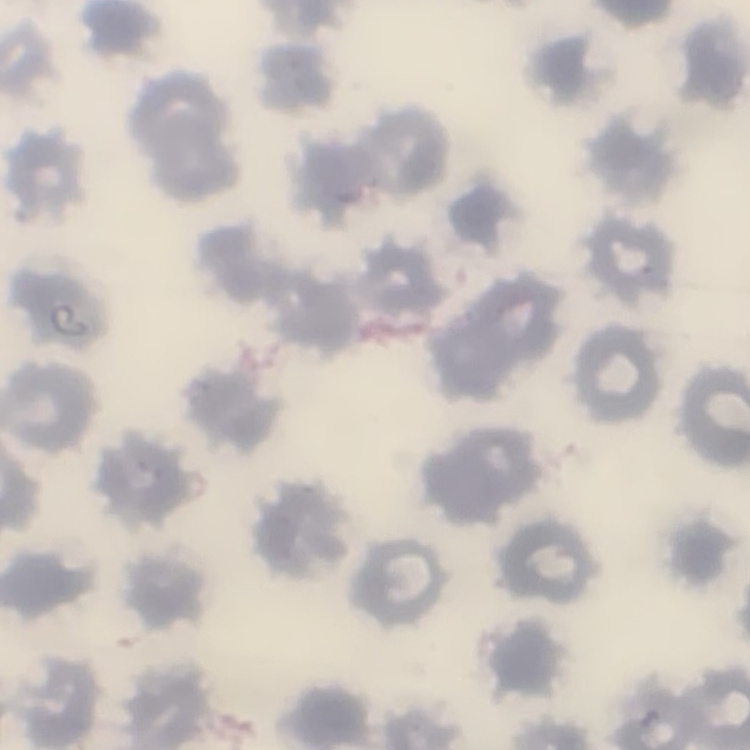

red blood cell morphology = no rouleaux formation
stain = Field's or Giemsa
image type = square crop of a larger photomicrograph
preparation = thin peripheral smear